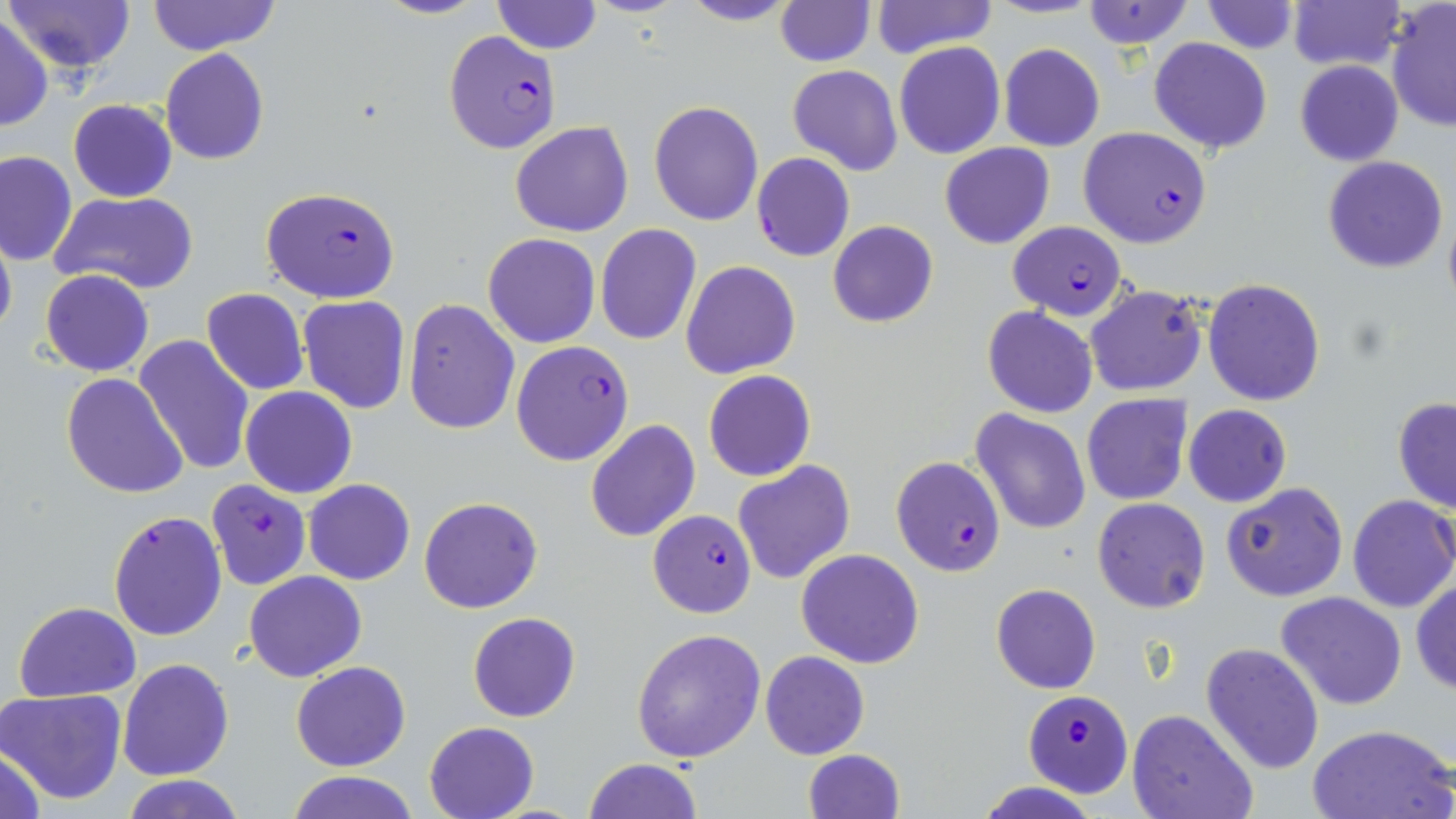

Approximate bounding boxes as (x1, y1, x2, y2) in pixels. Uninfected red blood cell locations: (5, 0, 133, 71), (147, 0, 279, 55), (371, 0, 491, 20), (676, 0, 802, 27), (984, 0, 1102, 19), (1079, 0, 1196, 50), (1199, 0, 1300, 54), (1285, 0, 1404, 73), (492, 1, 601, 54), (772, 1, 875, 66), (870, 1, 997, 57), (1386, 3, 1456, 131), (0, 7, 97, 113), (0, 15, 52, 131), (1148, 38, 1273, 153), (894, 41, 1006, 159), (998, 43, 1105, 151), (160, 48, 269, 165), (1296, 61, 1403, 166), (787, 64, 902, 175), (67, 100, 178, 201), (648, 100, 763, 226), (511, 121, 634, 237), (940, 142, 1054, 249), (0, 150, 77, 266), (1323, 155, 1449, 274), (51, 191, 199, 296), (827, 219, 938, 328), (0, 223, 17, 342), (595, 224, 703, 346), (484, 233, 599, 349), (680, 260, 801, 380), (40, 269, 154, 377), (1203, 279, 1325, 406), (1084, 283, 1207, 396), (202, 288, 309, 395), (298, 295, 412, 415), (403, 299, 520, 434), (982, 306, 1099, 417), (133, 335, 255, 476), (704, 370, 816, 482), (61, 372, 188, 500), (240, 386, 357, 498), (1082, 394, 1192, 506), (1392, 397, 1456, 513), (1182, 404, 1292, 508), (971, 408, 1092, 534), (585, 420, 700, 542), (732, 460, 856, 586), (303, 478, 415, 585), (1220, 482, 1348, 601), (1347, 495, 1456, 613), (419, 496, 544, 614), (1092, 497, 1211, 613), (795, 549, 925, 668), (243, 570, 367, 682), (1411, 578, 1456, 696), (991, 583, 1100, 694), (1275, 591, 1407, 711), (13, 601, 141, 702), (468, 612, 581, 722), (632, 627, 766, 762), (1201, 642, 1325, 773), (760, 650, 869, 759), (118, 658, 233, 781), (290, 661, 411, 771), (2, 690, 126, 803), (1126, 707, 1259, 819), (423, 720, 540, 818), (1307, 723, 1453, 819), (1, 742, 49, 819), (801, 748, 905, 819), (582, 758, 703, 818), (287, 772, 416, 819), (118, 776, 250, 818), (974, 783, 1099, 818). Plasmodium falciparum-infected red blood cell locations: (442, 30, 561, 153), (1078, 127, 1211, 248), (751, 152, 855, 262), (259, 185, 402, 304), (1012, 224, 1127, 321), (511, 341, 635, 467), (890, 455, 1007, 577), (206, 480, 311, 590), (648, 507, 757, 620), (108, 511, 227, 641), (1025, 692, 1131, 797). Slide-level diagnosis: Plasmodium falciparum. 1000x magnification. Optical microscopy. Image is 1456×819 pixels. Thin blood film. May-Grünwald-Giemsa stain. One field of a larger specimen.